Outline each Plasmodium ovale-infected red blood cell.
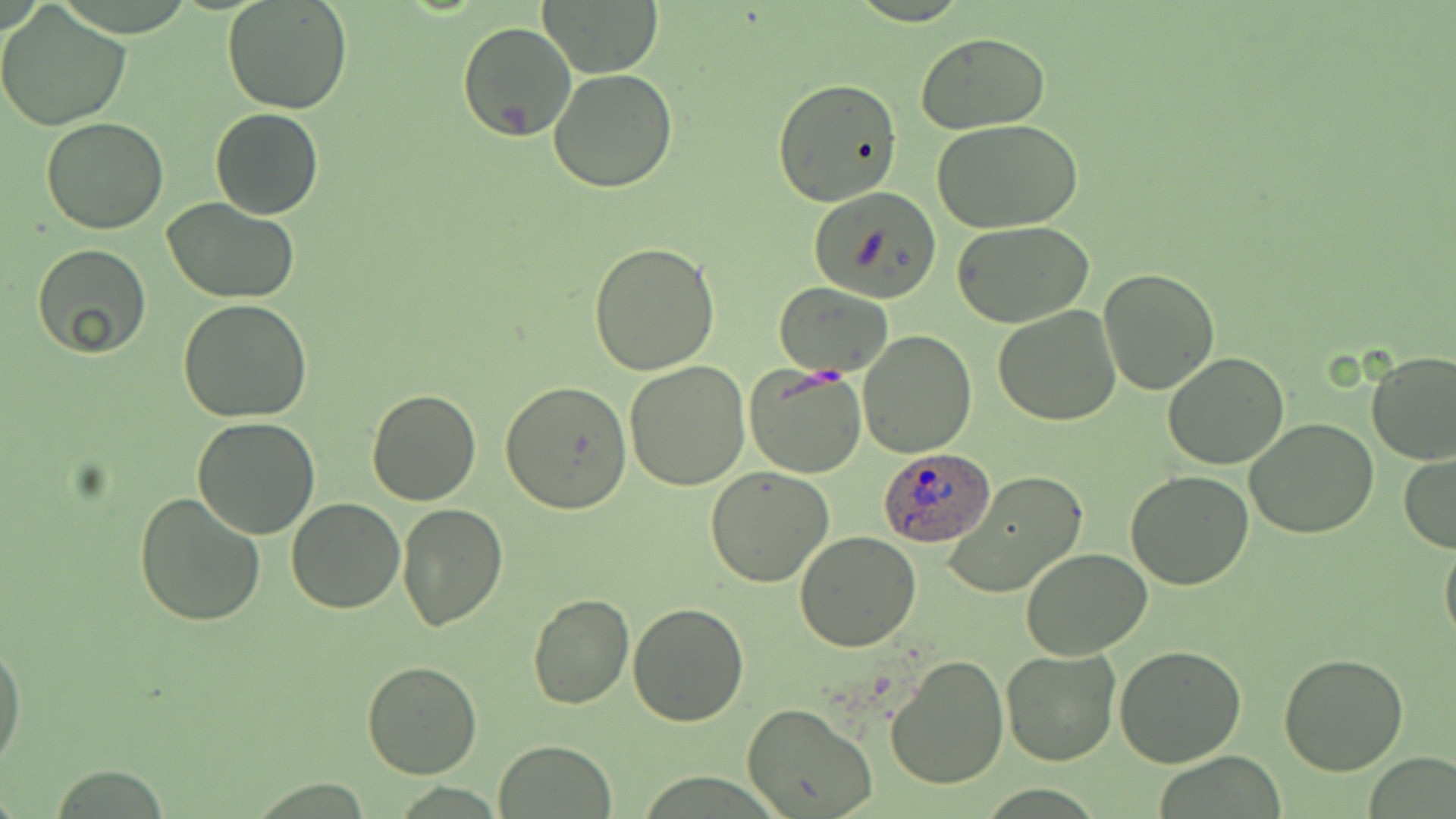

Approximate bounding boxes as (x1, y1, x2, y2) in pixels.
Plasmodium ovale-infected red blood cells: (879, 446, 994, 549).

Summary:
  - Uninfected red blood cell locations: (222, 0, 353, 115), (538, 0, 665, 77), (0, 4, 132, 132), (457, 21, 577, 143), (916, 32, 1052, 132), (547, 69, 677, 193), (772, 77, 904, 209), (210, 107, 324, 220), (41, 118, 170, 234), (934, 119, 1084, 234), (809, 186, 943, 303), (163, 198, 299, 305), (951, 220, 1094, 328), (587, 242, 720, 376), (31, 244, 152, 359), (1097, 268, 1220, 395), (774, 284, 892, 378), (177, 299, 313, 423), (992, 306, 1121, 426), (858, 330, 976, 459), (1162, 352, 1290, 471), (1366, 352, 1456, 465), (624, 359, 751, 490), (744, 363, 867, 479), (500, 381, 632, 513), (367, 390, 481, 507), (191, 417, 322, 539), (1244, 418, 1378, 539), (1399, 452, 1456, 553), (706, 468, 836, 587), (1126, 469, 1254, 590), (944, 471, 1090, 600), (134, 489, 266, 628), (287, 498, 405, 614), (395, 502, 509, 632), (1440, 527, 1456, 652), (793, 531, 921, 651), (1020, 546, 1153, 659), (527, 593, 634, 708), (625, 602, 749, 725), (0, 638, 24, 777), (1114, 644, 1245, 767), (1000, 647, 1122, 766), (884, 653, 1009, 791), (1276, 653, 1408, 775), (361, 661, 481, 778), (742, 703, 878, 819), (495, 739, 616, 818), (46, 766, 174, 817)
  - Slide-level diagnosis: Plasmodium ovale
  - Modality: optical microscopy
  - Magnification: 1000x
  - Field of view: one of a larger specimen
  - Preparation: thin blood smear
  - Stain: May-Grünwald-Giemsa
  - Image size: 1456×819 pixels